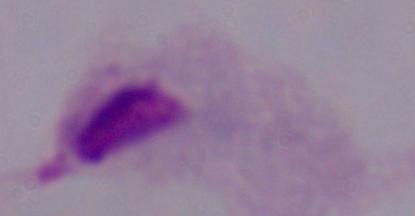

Summary:
  - Identification: trichomonad
  - Magnification: 1000x
  - Modality: micrograph